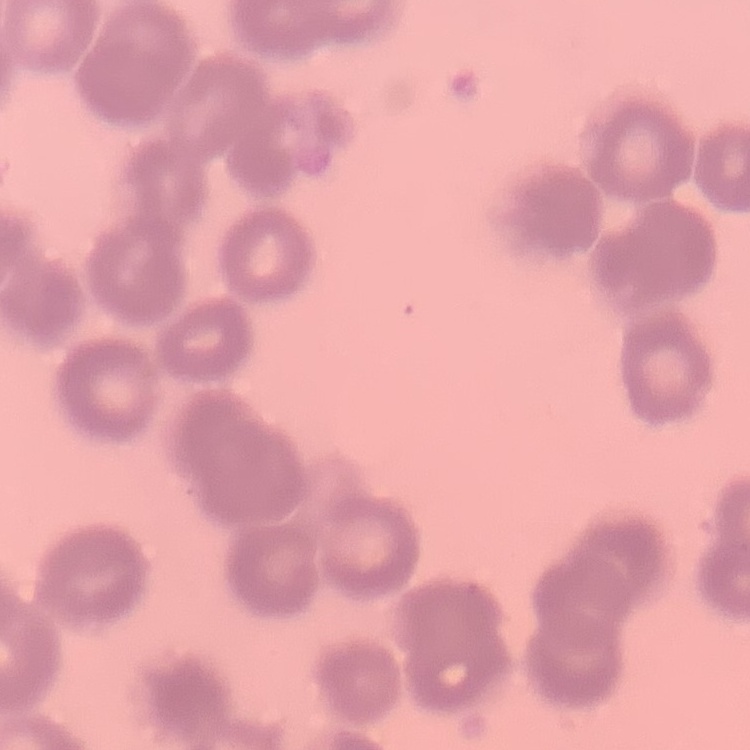
The erythrocytes exhibit rouleaux formation. Thin peripheral smear. One tile cut from a larger photomicrograph. Stained with either Field's or Giemsa.